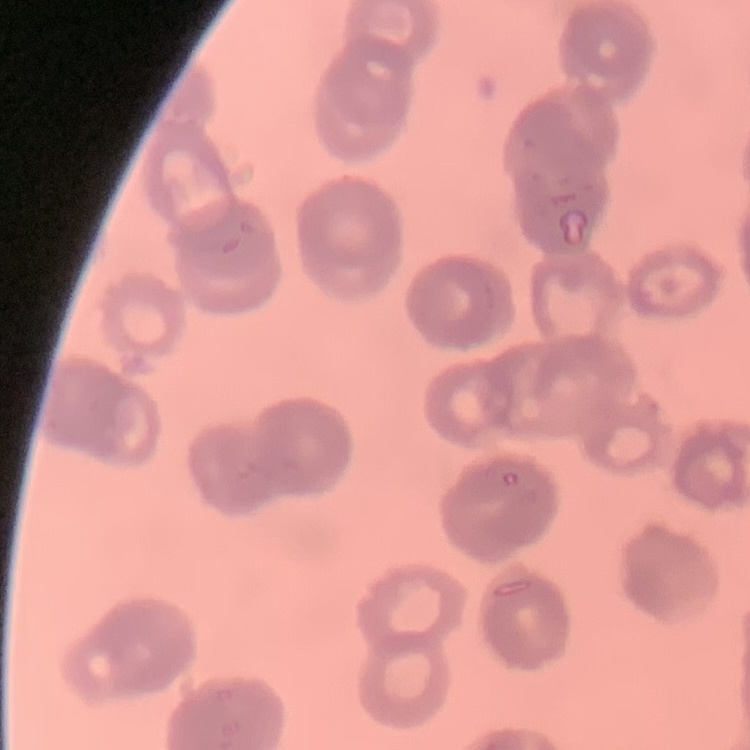 The red blood cells exhibit rouleaux formation. Stained with either Field's or Giemsa. Thin blood film. One tile cut from a larger photomicrograph.